Assess this cell for malaria.
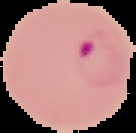
Parasitized.

From a thin blood film. The area outside the segmented cell region is set to black. Image is 136×133 pixels.